Name the blood parasite species.
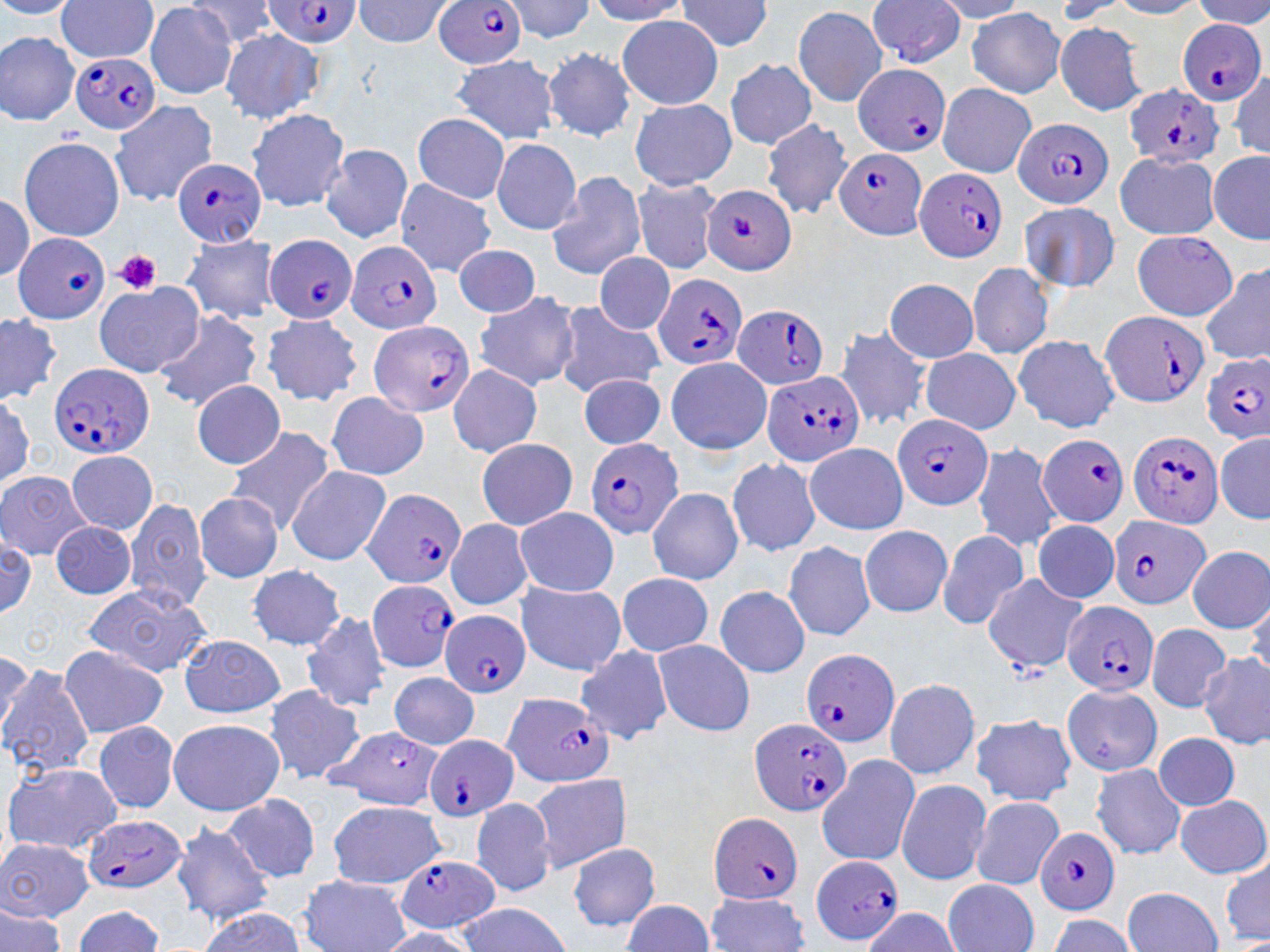
Plasmodium falciparum.

image size = 1270×952 pixels
field of view = single
magnification = 1000x
Plasmodium falciparum-infected red blood cell locations = approximate bounding boxes as named x1/y1/x2/y2 corners in pixels: (x1=432, y1=0, x2=534, y2=72), (x1=264, y1=2, x2=358, y2=48), (x1=1178, y1=18, x2=1258, y2=103), (x1=72, y1=52, x2=163, y2=136), (x1=849, y1=60, x2=950, y2=156), (x1=1127, y1=85, x2=1223, y2=167), (x1=1012, y1=114, x2=1117, y2=206), (x1=829, y1=148, x2=928, y2=239), (x1=167, y1=155, x2=266, y2=245), (x1=916, y1=166, x2=1008, y2=263), (x1=700, y1=181, x2=796, y2=274), (x1=267, y1=232, x2=358, y2=324), (x1=14, y1=233, x2=109, y2=322), (x1=348, y1=237, x2=446, y2=330), (x1=655, y1=273, x2=749, y2=369), (x1=733, y1=303, x2=829, y2=390), (x1=1102, y1=308, x2=1210, y2=409), (x1=367, y1=317, x2=476, y2=419), (x1=1197, y1=352, x2=1270, y2=445), (x1=52, y1=358, x2=152, y2=457), (x1=767, y1=373, x2=863, y2=468), (x1=890, y1=415, x2=993, y2=511), (x1=1130, y1=426, x2=1223, y2=524), (x1=1039, y1=432, x2=1130, y2=525), (x1=583, y1=438, x2=687, y2=539), (x1=358, y1=491, x2=464, y2=593), (x1=1104, y1=514, x2=1210, y2=613), (x1=369, y1=578, x2=463, y2=673), (x1=1059, y1=596, x2=1156, y2=694), (x1=441, y1=613, x2=530, y2=697), (x1=804, y1=643, x2=899, y2=741), (x1=501, y1=692, x2=611, y2=787), (x1=748, y1=718, x2=845, y2=816), (x1=425, y1=737, x2=519, y2=823), (x1=708, y1=813, x2=804, y2=905), (x1=83, y1=819, x2=191, y2=894), (x1=1035, y1=825, x2=1118, y2=917), (x1=804, y1=854, x2=909, y2=947), (x1=393, y1=856, x2=499, y2=935)
uninfected red blood cell locations = approximate bounding boxes as named x1/y1/x2/y2 corners in pixels: (x1=55, y1=0, x2=161, y2=60), (x1=357, y1=0, x2=449, y2=53), (x1=862, y1=0, x2=968, y2=62), (x1=142, y1=5, x2=242, y2=102), (x1=794, y1=6, x2=886, y2=104), (x1=965, y1=9, x2=1067, y2=99), (x1=613, y1=16, x2=725, y2=113), (x1=1055, y1=24, x2=1150, y2=117), (x1=219, y1=28, x2=323, y2=124), (x1=0, y1=29, x2=77, y2=129), (x1=546, y1=45, x2=636, y2=146), (x1=453, y1=53, x2=555, y2=147), (x1=728, y1=60, x2=823, y2=152), (x1=936, y1=83, x2=1033, y2=178), (x1=628, y1=100, x2=735, y2=189), (x1=111, y1=105, x2=208, y2=203), (x1=241, y1=111, x2=346, y2=213), (x1=416, y1=113, x2=508, y2=206), (x1=761, y1=121, x2=854, y2=218), (x1=21, y1=136, x2=129, y2=234), (x1=492, y1=138, x2=582, y2=238), (x1=320, y1=146, x2=415, y2=243), (x1=1209, y1=149, x2=1270, y2=243), (x1=1116, y1=152, x2=1222, y2=235), (x1=545, y1=169, x2=645, y2=284), (x1=391, y1=175, x2=500, y2=278), (x1=632, y1=175, x2=717, y2=272), (x1=1019, y1=195, x2=1121, y2=297), (x1=1130, y1=231, x2=1241, y2=322), (x1=179, y1=235, x2=280, y2=322), (x1=451, y1=241, x2=545, y2=322), (x1=594, y1=253, x2=678, y2=331), (x1=970, y1=261, x2=1052, y2=362), (x1=1207, y1=266, x2=1270, y2=365), (x1=883, y1=281, x2=979, y2=363), (x1=94, y1=284, x2=205, y2=379), (x1=477, y1=288, x2=586, y2=394), (x1=556, y1=297, x2=672, y2=394), (x1=149, y1=309, x2=262, y2=415), (x1=0, y1=312, x2=61, y2=407), (x1=261, y1=313, x2=361, y2=410), (x1=833, y1=326, x2=929, y2=417), (x1=1015, y1=334, x2=1126, y2=428), (x1=922, y1=342, x2=1028, y2=429), (x1=667, y1=359, x2=770, y2=456), (x1=450, y1=366, x2=544, y2=463), (x1=577, y1=373, x2=668, y2=452), (x1=193, y1=381, x2=288, y2=471), (x1=325, y1=390, x2=428, y2=480), (x1=229, y1=425, x2=334, y2=534), (x1=1216, y1=435, x2=1270, y2=523), (x1=479, y1=438, x2=580, y2=533), (x1=973, y1=442, x2=1061, y2=551), (x1=807, y1=443, x2=909, y2=539), (x1=65, y1=451, x2=160, y2=534), (x1=727, y1=455, x2=828, y2=563), (x1=288, y1=466, x2=391, y2=564), (x1=0, y1=473, x2=92, y2=567), (x1=644, y1=487, x2=745, y2=587), (x1=195, y1=491, x2=287, y2=585), (x1=128, y1=498, x2=214, y2=619), (x1=517, y1=506, x2=622, y2=596), (x1=446, y1=518, x2=535, y2=610), (x1=1029, y1=521, x2=1122, y2=603), (x1=54, y1=525, x2=140, y2=601), (x1=859, y1=527, x2=953, y2=619), (x1=938, y1=530, x2=1028, y2=628), (x1=784, y1=535, x2=871, y2=640), (x1=1187, y1=547, x2=1270, y2=634), (x1=247, y1=562, x2=344, y2=655), (x1=619, y1=570, x2=715, y2=660), (x1=981, y1=575, x2=1084, y2=667), (x1=515, y1=579, x2=626, y2=676), (x1=716, y1=582, x2=813, y2=680), (x1=81, y1=583, x2=216, y2=676), (x1=300, y1=610, x2=393, y2=713), (x1=1148, y1=623, x2=1235, y2=717), (x1=653, y1=637, x2=756, y2=733), (x1=178, y1=638, x2=289, y2=716), (x1=56, y1=642, x2=167, y2=747), (x1=575, y1=644, x2=671, y2=730), (x1=1195, y1=651, x2=1270, y2=751), (x1=2, y1=660, x2=96, y2=782), (x1=388, y1=671, x2=478, y2=753), (x1=887, y1=676, x2=980, y2=776), (x1=1060, y1=680, x2=1162, y2=779), (x1=264, y1=682, x2=365, y2=789), (x1=970, y1=712, x2=1079, y2=808), (x1=168, y1=719, x2=285, y2=816), (x1=92, y1=723, x2=183, y2=815), (x1=317, y1=725, x2=450, y2=813), (x1=1153, y1=729, x2=1237, y2=810), (x1=828, y1=754, x2=921, y2=864), (x1=4, y1=763, x2=123, y2=854), (x1=1089, y1=763, x2=1185, y2=858), (x1=530, y1=774, x2=635, y2=877), (x1=899, y1=778, x2=990, y2=882), (x1=221, y1=795, x2=322, y2=885), (x1=1179, y1=796, x2=1265, y2=878), (x1=973, y1=797, x2=1065, y2=888), (x1=323, y1=801, x2=425, y2=888), (x1=467, y1=801, x2=557, y2=898), (x1=170, y1=816, x2=273, y2=930), (x1=1, y1=835, x2=94, y2=926), (x1=568, y1=840, x2=660, y2=930), (x1=1217, y1=859, x2=1270, y2=945), (x1=298, y1=871, x2=413, y2=952), (x1=939, y1=876, x2=1036, y2=952), (x1=1125, y1=888, x2=1221, y2=952), (x1=704, y1=895, x2=810, y2=952), (x1=452, y1=902, x2=571, y2=952), (x1=74, y1=908, x2=169, y2=950)
modality = light microscopy
stain = May-Grünwald-Giemsa
platelet locations = approximate bounding boxes as named x1/y1/x2/y2 corners in pixels: (x1=113, y1=249, x2=166, y2=293)
preparation = thin blood film